Give the extent of all Plasmodium falciparum-infected red blood cells.
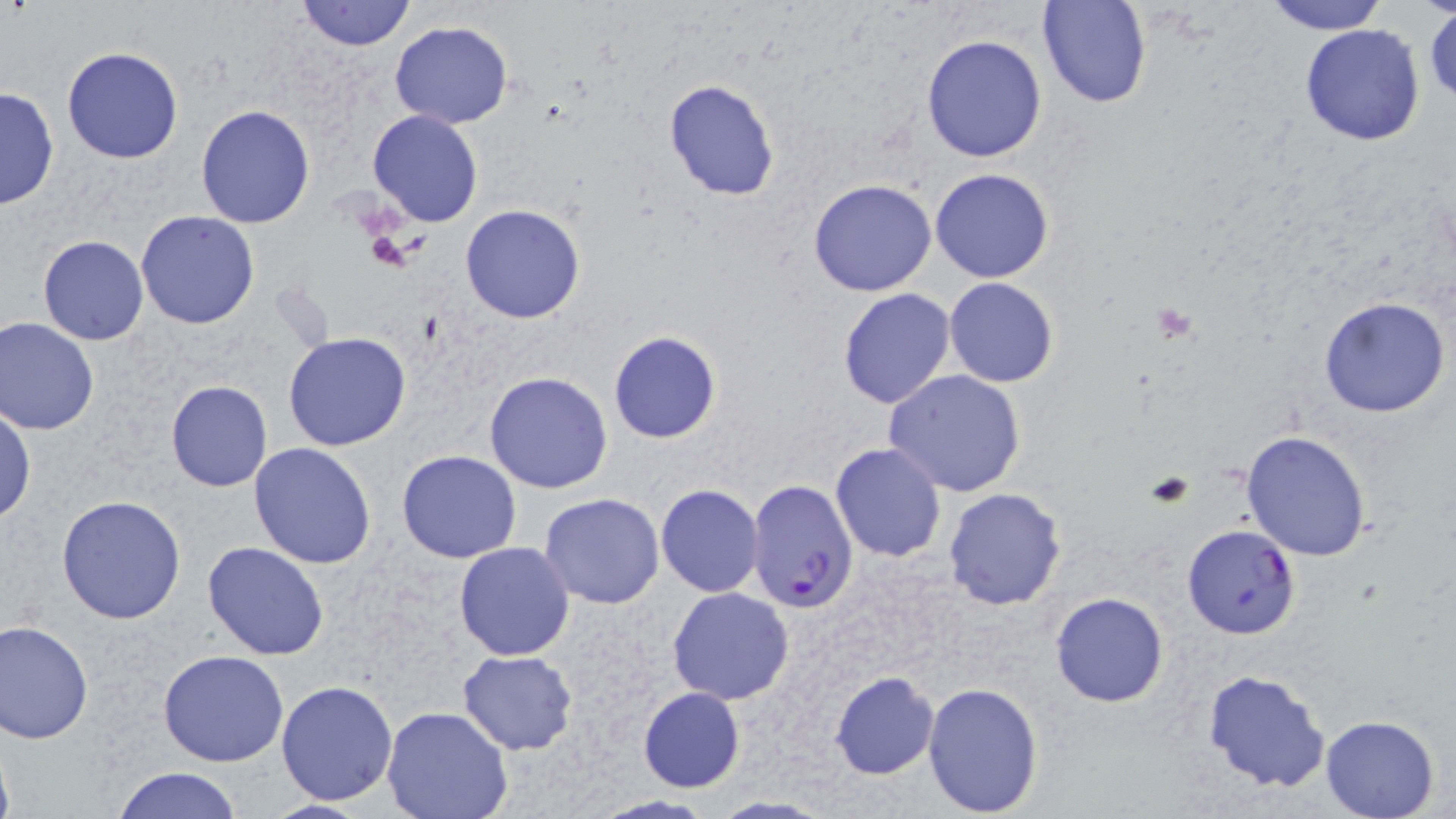
Approximate bounding boxes as (x1, y1, x2, y2) in pixels.
Plasmodium falciparum-infected red blood cells: (746, 479, 862, 612).

{
  "slide_level_diagnosis": "Plasmodium falciparum",
  "platelet_locations": "approximate bounding boxes as (x1, y1, x2, y2) in pixels: (365, 230, 416, 272), (1151, 304, 1199, 342)",
  "field_of_view": "one of a larger specimen",
  "uninfected_red_blood_cell_locations": "approximate bounding boxes as (x1, y1, x2, y2) in pixels: (295, 0, 417, 51), (1037, 0, 1151, 109), (1261, 0, 1387, 35), (1424, 5, 1456, 108), (391, 21, 511, 129), (1298, 24, 1427, 147), (921, 34, 1047, 163), (61, 47, 185, 164), (662, 79, 781, 201), (0, 84, 60, 212), (195, 103, 316, 229), (367, 110, 485, 228), (930, 168, 1055, 283), (808, 179, 938, 297), (459, 204, 586, 324), (135, 210, 261, 329), (38, 236, 149, 346), (943, 277, 1059, 387), (837, 288, 958, 408), (1317, 296, 1450, 418), (0, 317, 100, 435), (283, 332, 411, 451), (607, 332, 722, 443), (884, 369, 1028, 498), (485, 371, 614, 494), (166, 381, 273, 492), (0, 406, 35, 524), (1240, 430, 1372, 562), (250, 442, 378, 568), (829, 443, 947, 563), (397, 450, 523, 564), (656, 484, 764, 597), (943, 487, 1067, 610), (539, 494, 664, 609), (56, 495, 187, 625), (1182, 524, 1301, 640), (202, 542, 330, 660), (454, 542, 575, 660), (668, 587, 795, 705), (1050, 592, 1169, 708), (0, 619, 96, 744), (158, 649, 290, 766), (458, 651, 579, 754), (1202, 668, 1331, 794), (830, 670, 940, 780), (922, 679, 1043, 816), (277, 681, 398, 805), (637, 688, 745, 793), (381, 704, 512, 819), (1319, 715, 1439, 819), (108, 766, 243, 819), (582, 795, 721, 817), (258, 800, 378, 817)",
  "magnification": "1000x",
  "preparation": "thin blood film",
  "stain": "May-Grünwald-Giemsa",
  "modality": "optical microscopy",
  "image_size": "1456×819 pixels"
}